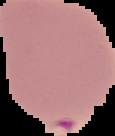
image type = cell region segmented out of the field of view; surrounding area masked to black
preparation = thin blood smear
malaria status = parasitized
image size = 115×136 pixels